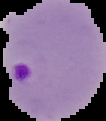

image_type: segmented cell region on a black background
result: malaria parasites detected
image_size: 106×121 pixels
preparation: thin blood smear